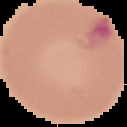

preparation = thin blood smear
image size = 127×127 pixels
result = malaria parasites identified
image type = cell region segmented out of the field of view; surrounding area masked to black